Comment on the morphology of the erythrocytes.
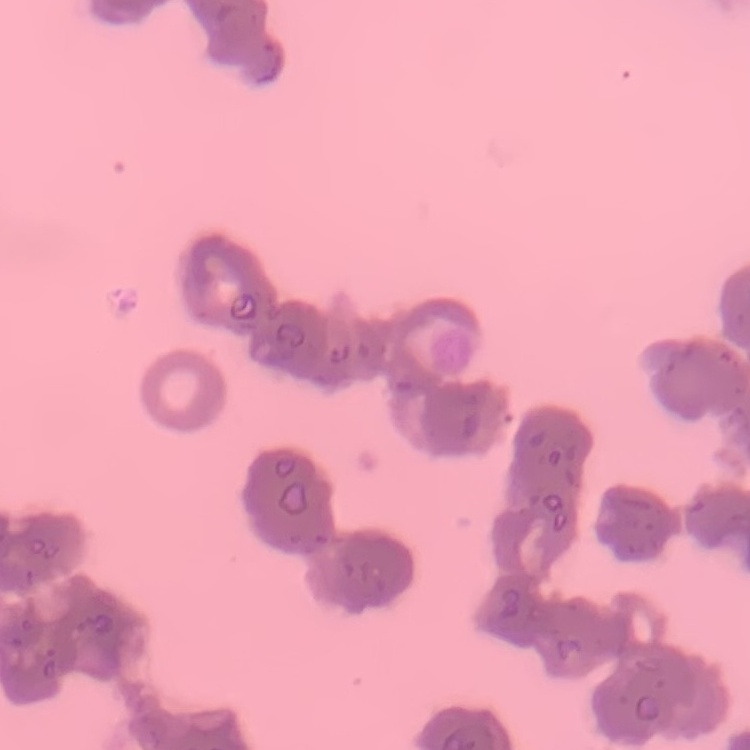

Rouleaux formation.

One tile cut from a larger photomicrograph. Thin peripheral smear. Stained with either Field's or Giemsa.